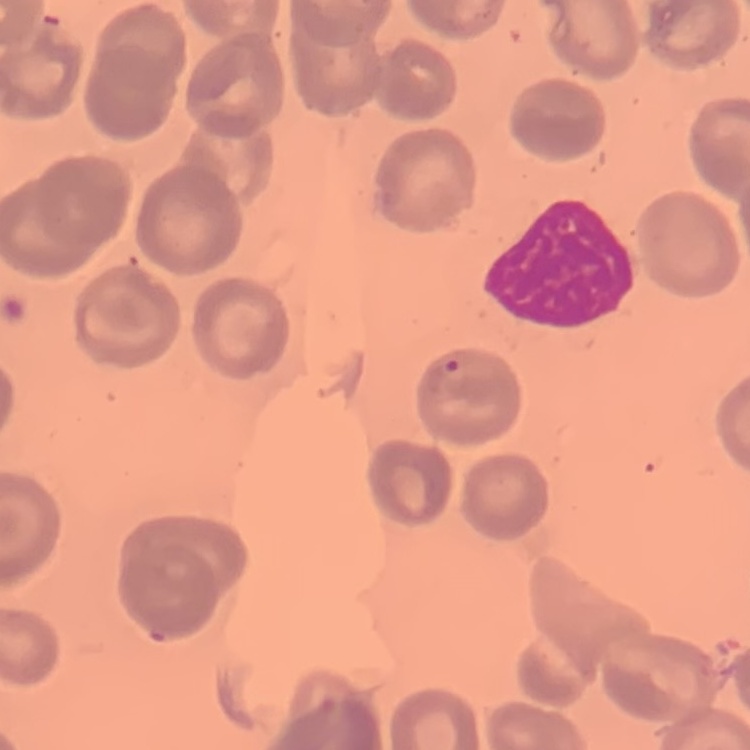

red blood cell morphology = no rouleaux formation
stain = Field's or Giemsa
preparation = thin blood smear
image type = one tile cut from a larger photomicrograph